Classify this cell by malaria status.
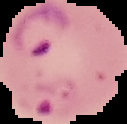
Parasitized.

preparation: thin blood smear
image_size: 127×124 pixels
image_type: segmented cell region on a black background